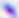

Micrograph. Toxoplasma gondii is seen. 400x magnification.